Report the malaria status of this cell.
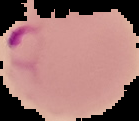

It is parasitized.

Segmented cell region on a black background. Image is 139×121 pixels. From a thin blood smear.